Evaluate for Plasmodium parasites.
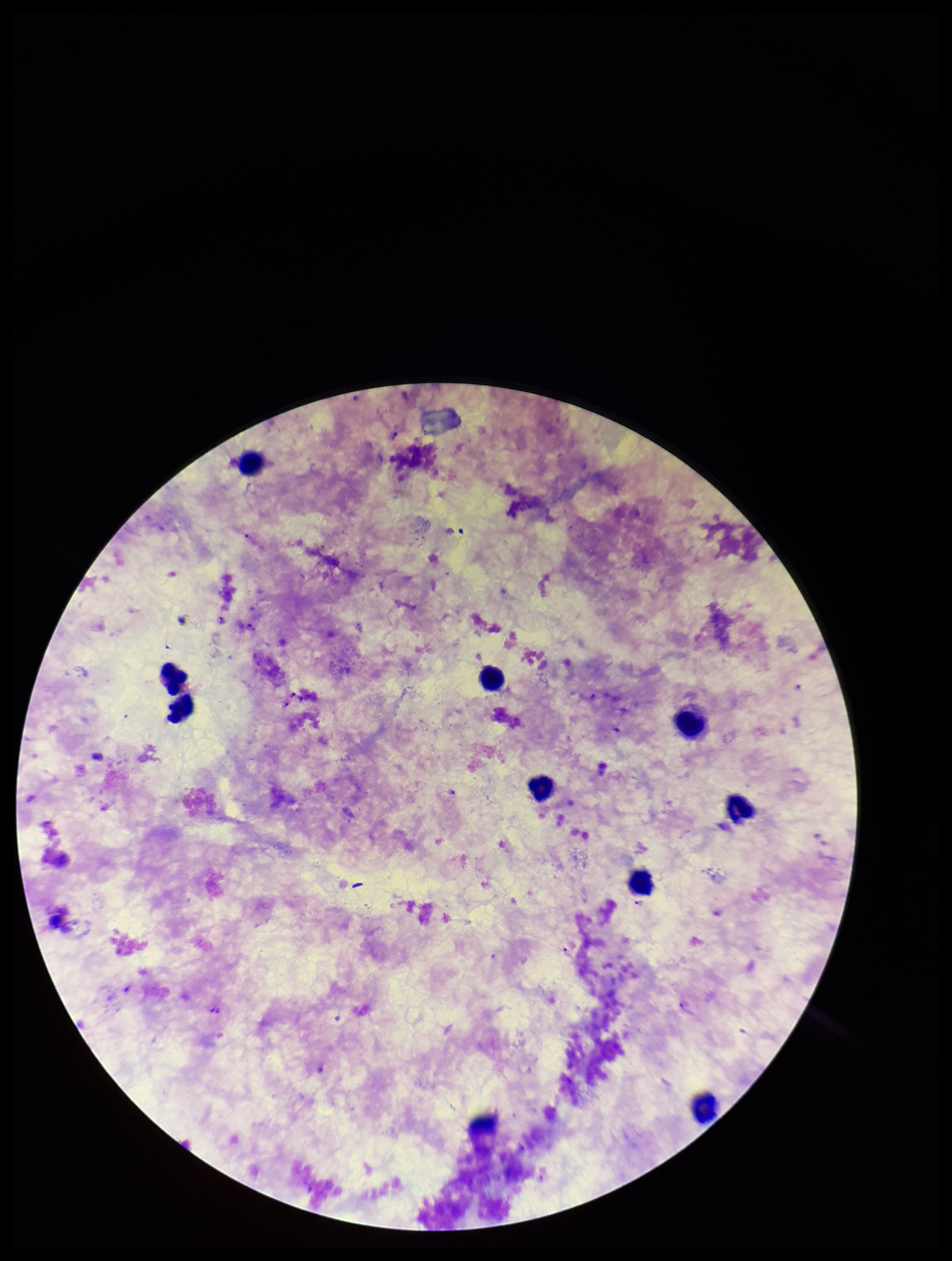
Detected.

Summary:
  - Patient malaria status: infected
  - Stain: Giemsa
  - Species reported for this patient: Plasmodium falciparum
  - Preparation: thick blood smear
  - Leukocyte count: 9
  - Parasite count: 4
  - Field of view: single
  - Capture: smartphone photograph through the microscope eyepiece
  - Image size: 952×1261 pixels